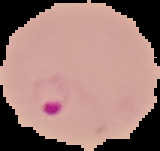

result: malaria parasites identified
image_type: segmented cell region with the area outside set to black
preparation: thin blood smear
image_size: 160×151 pixels